Classify this cell by malaria status.
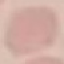

Uninfected.

Automatically extracted cell patch, resized to 64 × 64 pixels. Giemsa stain. Thin blood smear. Acquired by smartphone through the microscope eyepiece.